State the blood parasite species.
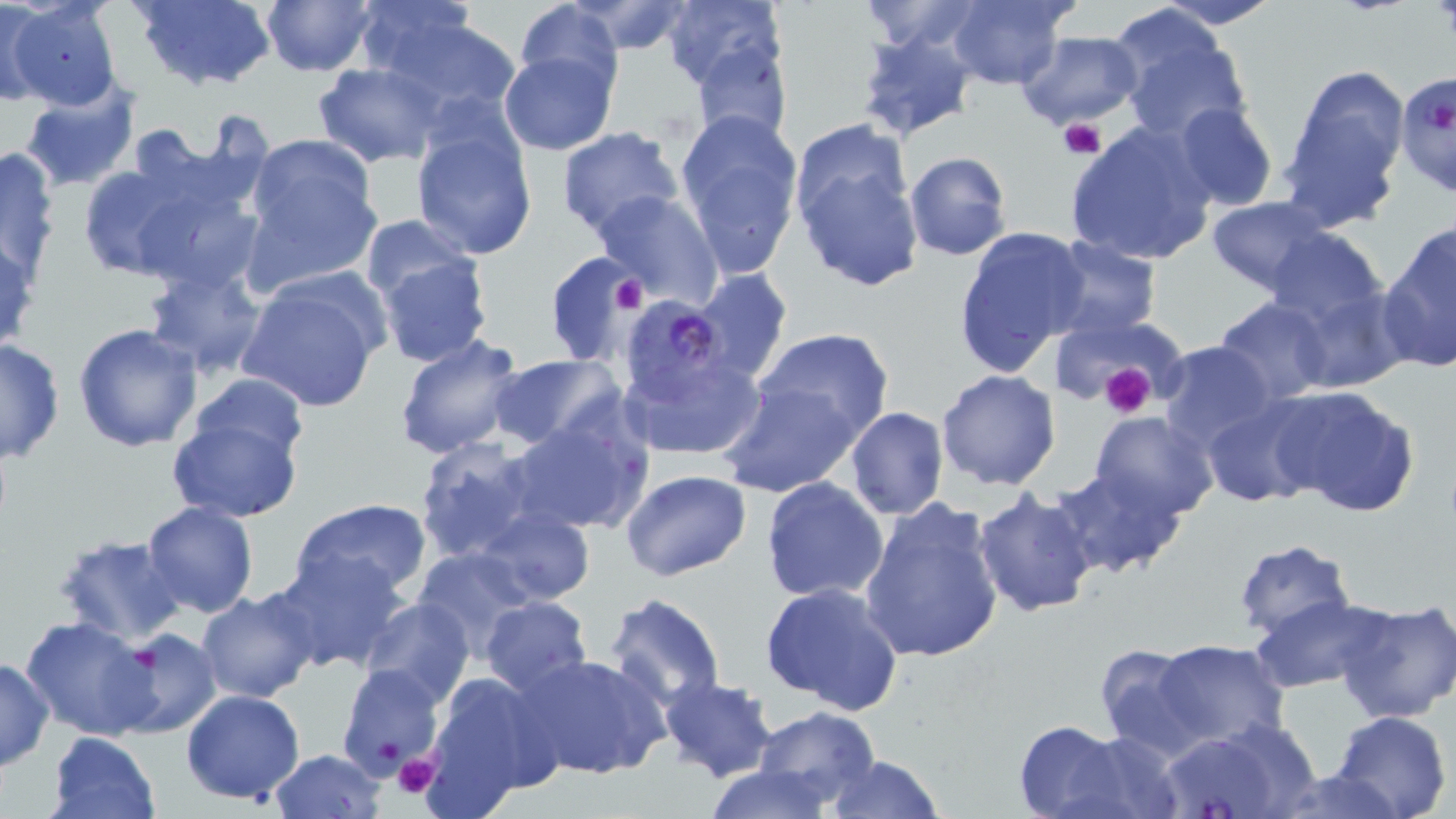

Plasmodium falciparum.

Approximate bounding boxes as named x1/y1/x2/y2 corners in pixels. Plasmodium falciparum-infected red blood cell locations: (x1=1393, y1=70, x2=1456, y2=198), (x1=630, y1=297, x2=734, y2=404). Platelet locations: (x1=1059, y1=117, x2=1106, y2=161), (x1=612, y1=275, x2=647, y2=314), (x1=1095, y1=363, x2=1159, y2=418), (x1=391, y1=752, x2=441, y2=799). Uninfected red blood cell locations: (x1=0, y1=0, x2=48, y2=105), (x1=131, y1=0, x2=278, y2=90), (x1=260, y1=0, x2=376, y2=76), (x1=348, y1=0, x2=482, y2=87), (x1=944, y1=0, x2=1076, y2=90), (x1=1150, y1=0, x2=1284, y2=29), (x1=515, y1=1, x2=621, y2=95), (x1=572, y1=1, x2=691, y2=55), (x1=857, y1=1, x2=988, y2=54), (x1=6, y1=2, x2=123, y2=110), (x1=662, y1=2, x2=785, y2=90), (x1=374, y1=15, x2=524, y2=123), (x1=1114, y1=19, x2=1252, y2=142), (x1=854, y1=28, x2=979, y2=143), (x1=1014, y1=31, x2=1145, y2=129), (x1=688, y1=40, x2=793, y2=149), (x1=498, y1=50, x2=618, y2=155), (x1=315, y1=62, x2=441, y2=167), (x1=1279, y1=65, x2=1413, y2=225), (x1=20, y1=84, x2=140, y2=188), (x1=1173, y1=101, x2=1278, y2=213), (x1=674, y1=108, x2=805, y2=274), (x1=410, y1=118, x2=536, y2=261), (x1=1065, y1=121, x2=1217, y2=267), (x1=556, y1=127, x2=684, y2=241), (x1=241, y1=135, x2=381, y2=275), (x1=793, y1=140, x2=923, y2=291), (x1=1, y1=144, x2=62, y2=279), (x1=903, y1=151, x2=1011, y2=261), (x1=78, y1=164, x2=196, y2=280), (x1=118, y1=165, x2=266, y2=300), (x1=593, y1=189, x2=722, y2=306), (x1=1205, y1=196, x2=1333, y2=296), (x1=358, y1=215, x2=477, y2=307), (x1=1378, y1=222, x2=1456, y2=374), (x1=951, y1=227, x2=1088, y2=375), (x1=1263, y1=227, x2=1389, y2=330), (x1=1042, y1=236, x2=1161, y2=340), (x1=373, y1=250, x2=494, y2=370), (x1=544, y1=252, x2=640, y2=368), (x1=142, y1=264, x2=266, y2=377), (x1=692, y1=267, x2=795, y2=382), (x1=234, y1=274, x2=385, y2=414), (x1=1214, y1=297, x2=1332, y2=403), (x1=1053, y1=314, x2=1177, y2=401), (x1=73, y1=322, x2=203, y2=450), (x1=755, y1=326, x2=893, y2=439), (x1=393, y1=335, x2=527, y2=458), (x1=0, y1=337, x2=64, y2=463), (x1=1156, y1=341, x2=1280, y2=453), (x1=621, y1=351, x2=765, y2=461), (x1=488, y1=354, x2=624, y2=454), (x1=936, y1=369, x2=1062, y2=491), (x1=189, y1=370, x2=311, y2=464), (x1=717, y1=381, x2=862, y2=498), (x1=1269, y1=384, x2=1421, y2=519), (x1=1201, y1=397, x2=1326, y2=510), (x1=167, y1=403, x2=304, y2=523), (x1=844, y1=406, x2=949, y2=520), (x1=1088, y1=411, x2=1220, y2=524), (x1=504, y1=415, x2=650, y2=536), (x1=413, y1=435, x2=543, y2=564), (x1=1049, y1=466, x2=1185, y2=579), (x1=620, y1=469, x2=751, y2=581), (x1=759, y1=478, x2=889, y2=605), (x1=973, y1=490, x2=1100, y2=617), (x1=287, y1=498, x2=434, y2=605), (x1=858, y1=498, x2=1006, y2=665), (x1=142, y1=500, x2=258, y2=618), (x1=475, y1=506, x2=594, y2=607), (x1=438, y1=516, x2=586, y2=685), (x1=53, y1=532, x2=188, y2=643), (x1=1231, y1=540, x2=1358, y2=643), (x1=410, y1=547, x2=540, y2=663), (x1=270, y1=551, x2=407, y2=673), (x1=761, y1=583, x2=904, y2=716), (x1=197, y1=588, x2=319, y2=704), (x1=603, y1=591, x2=727, y2=713), (x1=1250, y1=595, x2=1385, y2=694), (x1=480, y1=596, x2=593, y2=699), (x1=357, y1=597, x2=476, y2=707), (x1=1334, y1=598, x2=1456, y2=725), (x1=20, y1=614, x2=156, y2=742), (x1=110, y1=627, x2=221, y2=738), (x1=1154, y1=639, x2=1291, y2=751), (x1=1094, y1=643, x2=1205, y2=759), (x1=516, y1=652, x2=671, y2=781), (x1=0, y1=657, x2=53, y2=770), (x1=334, y1=663, x2=445, y2=780), (x1=417, y1=670, x2=559, y2=815), (x1=659, y1=676, x2=777, y2=782), (x1=180, y1=690, x2=306, y2=805), (x1=754, y1=705, x2=881, y2=806), (x1=1331, y1=711, x2=1451, y2=819), (x1=1153, y1=720, x2=1314, y2=819), (x1=1012, y1=721, x2=1132, y2=819), (x1=47, y1=732, x2=161, y2=819), (x1=267, y1=749, x2=388, y2=819), (x1=823, y1=756, x2=946, y2=818), (x1=702, y1=765, x2=839, y2=819), (x1=1269, y1=767, x2=1399, y2=819). Image is 1456×819 pixels. Optical microscopy. May-Grünwald-Giemsa stain. 1000x magnification. One field of a larger specimen. Thin blood film.